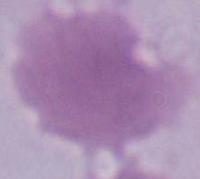 Photomicrograph. A red blood cell is shown. Captured at 1000x magnification.